Locate every Plasmodium parasite.
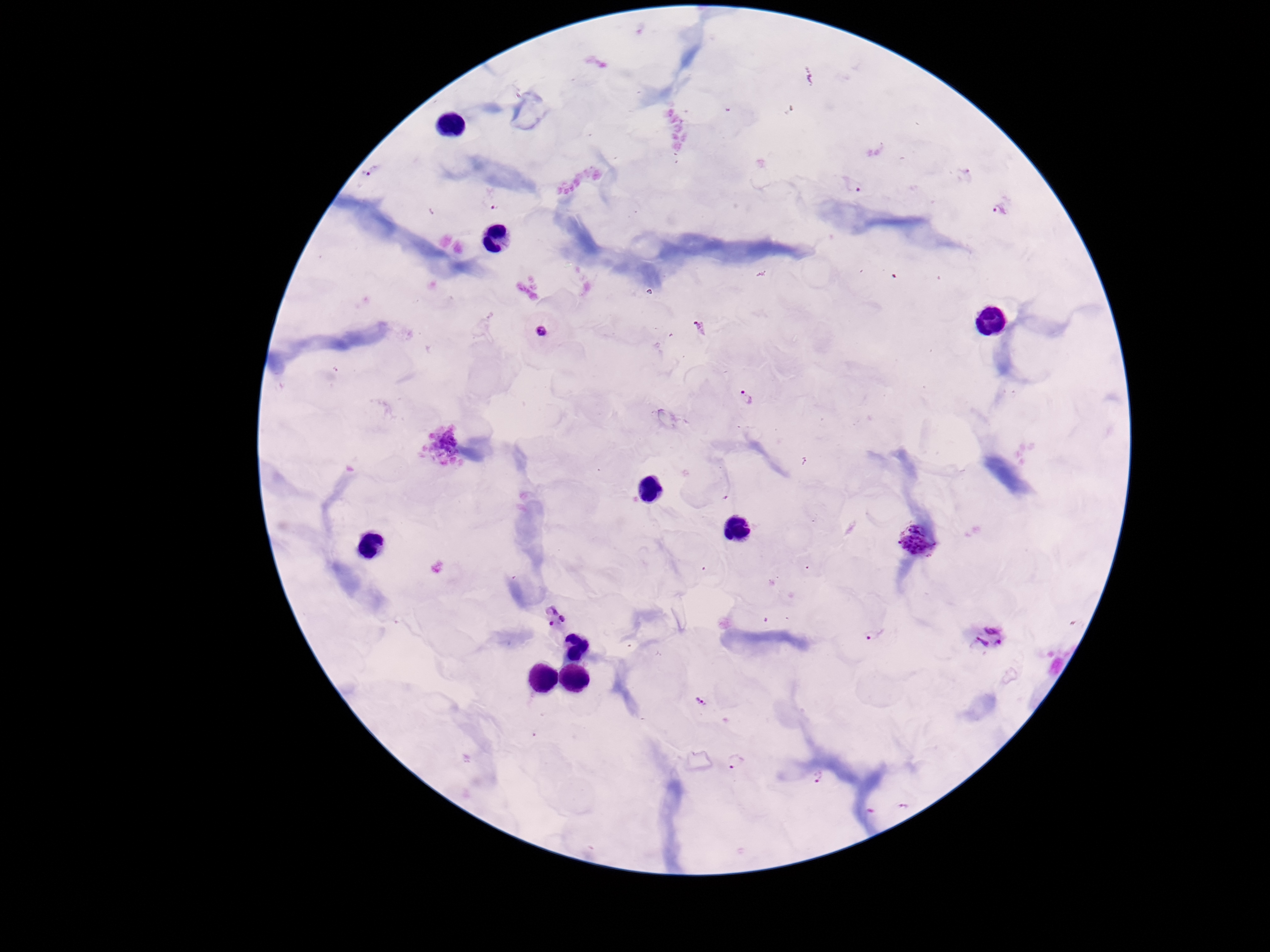

Approximate object centers, in pixels from the top-left corner.
Plasmodium parasites: (x=365, y=173), (x=854, y=184), (x=493, y=206), (x=999, y=210), (x=541, y=331), (x=748, y=396), (x=916, y=542), (x=555, y=617), (x=874, y=633), (x=988, y=639), (x=703, y=703), (x=734, y=762), (x=818, y=776), (x=905, y=807).

preparation = thick peripheral-blood smear
capture = smartphone camera through the microscope eyepiece
patient malaria status = positive
field of view = single
stain = Giemsa
magnification = 100x
image size = 1270×952 pixels